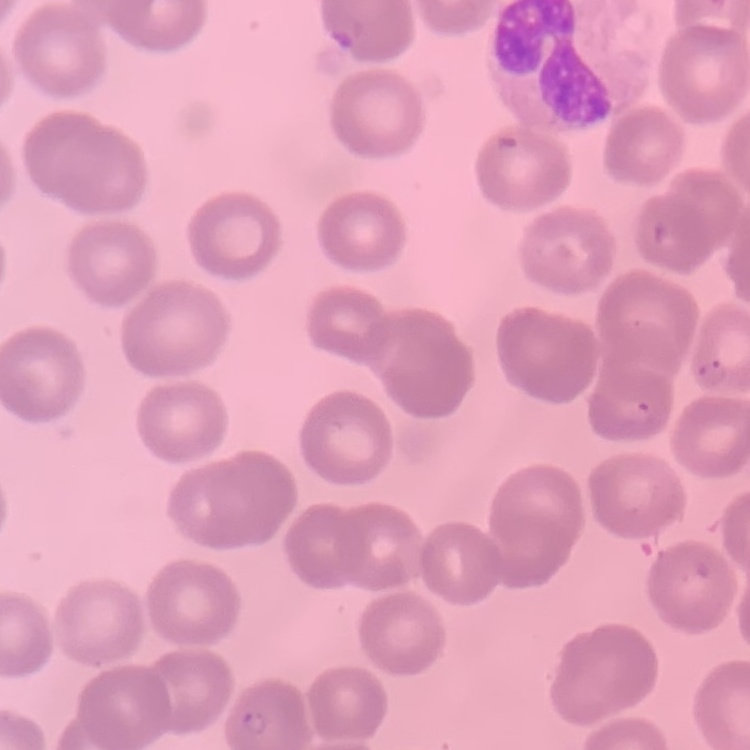
{
  "erythrocyte_morphology": "no rouleaux formation",
  "image_type": "one tile cut from a larger photomicrograph",
  "preparation": "thin blood smear",
  "stain": "Field's or Giemsa"
}